Identify the parasite.
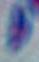

Toxoplasma gondii.

Summary:
  - Modality: micrograph
  - Magnification: 1000x